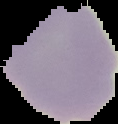

{
  "image_size": "118×124 pixels",
  "image_type": "segmented cell region with the area outside set to black",
  "malaria_status": "uninfected",
  "preparation": "thin blood film"
}